Locate and identify every blood parasite.
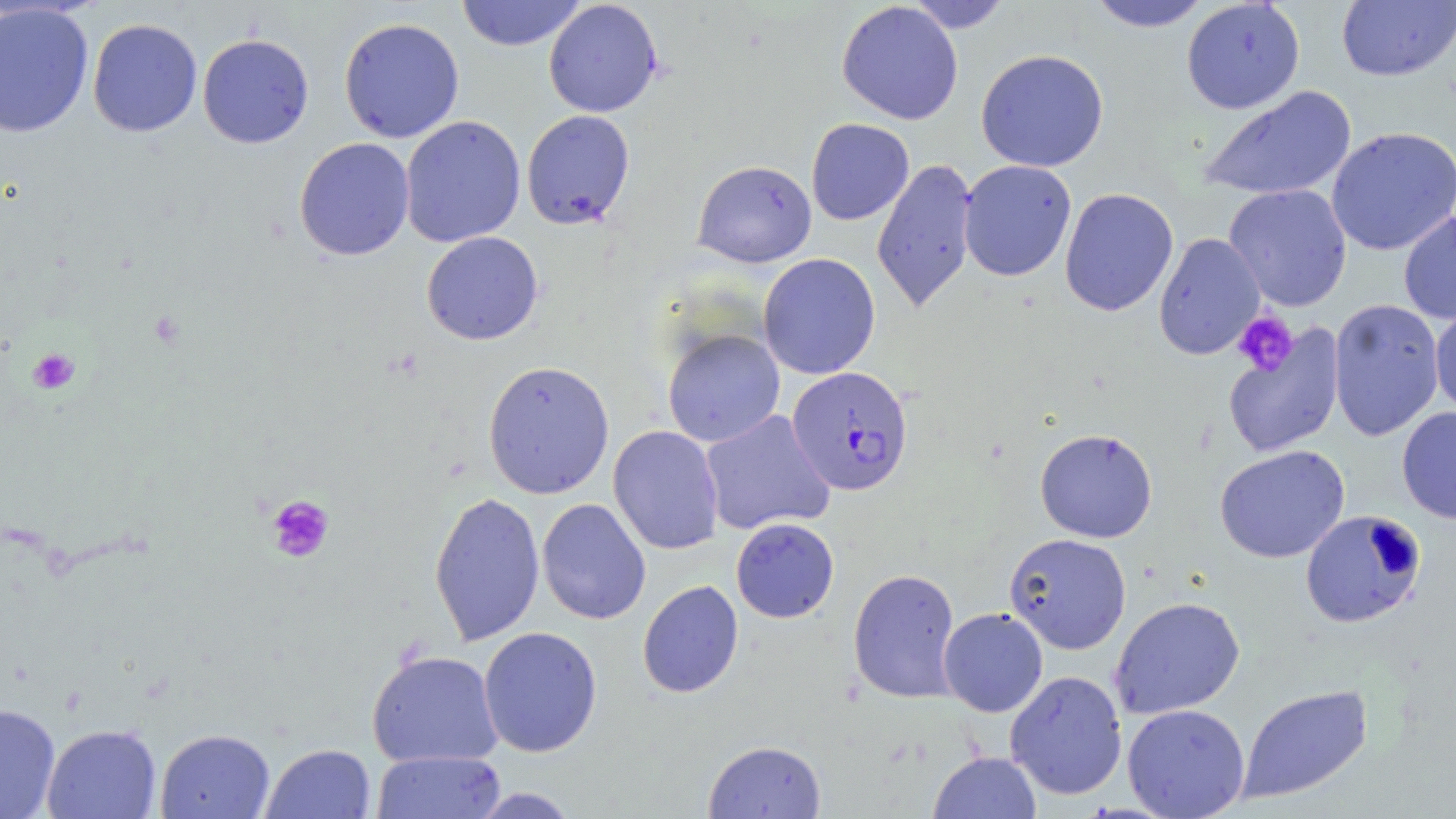

Approximate bounding boxes as named x1/y1/x2/y2 corners in pixels.
Plasmodium falciparum-infected red blood cells: (x1=786, y1=366, x2=914, y2=497).
No Plasmodium ovale, Plasmodium malariae, Plasmodium vivax, Babesia divergens, or Trypanosoma brucei observed.

Platelet locations: (x1=1231, y1=311, x2=1298, y2=375), (x1=27, y1=348, x2=81, y2=394), (x1=265, y1=494, x2=335, y2=563). Uninfected red blood cell locations: (x1=455, y1=0, x2=587, y2=52), (x1=543, y1=0, x2=663, y2=118), (x1=906, y1=0, x2=1013, y2=33), (x1=837, y1=1, x2=963, y2=125), (x1=1085, y1=1, x2=1212, y2=31), (x1=1180, y1=1, x2=1305, y2=114), (x1=1337, y1=1, x2=1456, y2=82), (x1=0, y1=3, x2=94, y2=138), (x1=338, y1=17, x2=465, y2=144), (x1=87, y1=18, x2=203, y2=137), (x1=197, y1=32, x2=314, y2=149), (x1=975, y1=48, x2=1109, y2=172), (x1=1198, y1=85, x2=1358, y2=201), (x1=521, y1=110, x2=635, y2=229), (x1=399, y1=115, x2=526, y2=248), (x1=806, y1=118, x2=914, y2=225), (x1=1326, y1=126, x2=1456, y2=256), (x1=293, y1=138, x2=415, y2=261), (x1=871, y1=157, x2=979, y2=313), (x1=692, y1=159, x2=817, y2=268), (x1=958, y1=159, x2=1077, y2=282), (x1=1223, y1=183, x2=1353, y2=312), (x1=1059, y1=187, x2=1179, y2=317), (x1=1398, y1=209, x2=1456, y2=325), (x1=421, y1=231, x2=543, y2=345), (x1=1153, y1=232, x2=1267, y2=360), (x1=757, y1=253, x2=880, y2=380), (x1=1328, y1=299, x2=1445, y2=442), (x1=1430, y1=304, x2=1456, y2=419), (x1=1222, y1=324, x2=1346, y2=458), (x1=662, y1=328, x2=785, y2=447), (x1=483, y1=360, x2=614, y2=499), (x1=1397, y1=406, x2=1456, y2=525), (x1=700, y1=410, x2=835, y2=535), (x1=608, y1=425, x2=724, y2=555), (x1=1034, y1=428, x2=1158, y2=543), (x1=1215, y1=444, x2=1349, y2=563), (x1=428, y1=490, x2=545, y2=647), (x1=536, y1=498, x2=651, y2=625), (x1=1300, y1=509, x2=1425, y2=628), (x1=731, y1=517, x2=839, y2=622), (x1=1004, y1=533, x2=1132, y2=654), (x1=847, y1=568, x2=961, y2=704), (x1=638, y1=580, x2=743, y2=698), (x1=1109, y1=596, x2=1246, y2=719), (x1=938, y1=607, x2=1048, y2=717), (x1=478, y1=626, x2=602, y2=757), (x1=366, y1=649, x2=503, y2=767), (x1=1005, y1=670, x2=1128, y2=800), (x1=1237, y1=683, x2=1373, y2=804), (x1=0, y1=703, x2=60, y2=819), (x1=1122, y1=703, x2=1250, y2=819), (x1=42, y1=723, x2=161, y2=819), (x1=155, y1=728, x2=275, y2=819), (x1=703, y1=740, x2=827, y2=818), (x1=261, y1=743, x2=375, y2=819), (x1=371, y1=750, x2=506, y2=819), (x1=928, y1=750, x2=1042, y2=819), (x1=468, y1=787, x2=581, y2=818). Slide-level diagnosis: Plasmodium falciparum. May-Grünwald-Giemsa-stained preparation. Image is 1456×819 pixels. Thin blood smear. 1000x magnification. Optical microscopy. One field of a larger specimen.